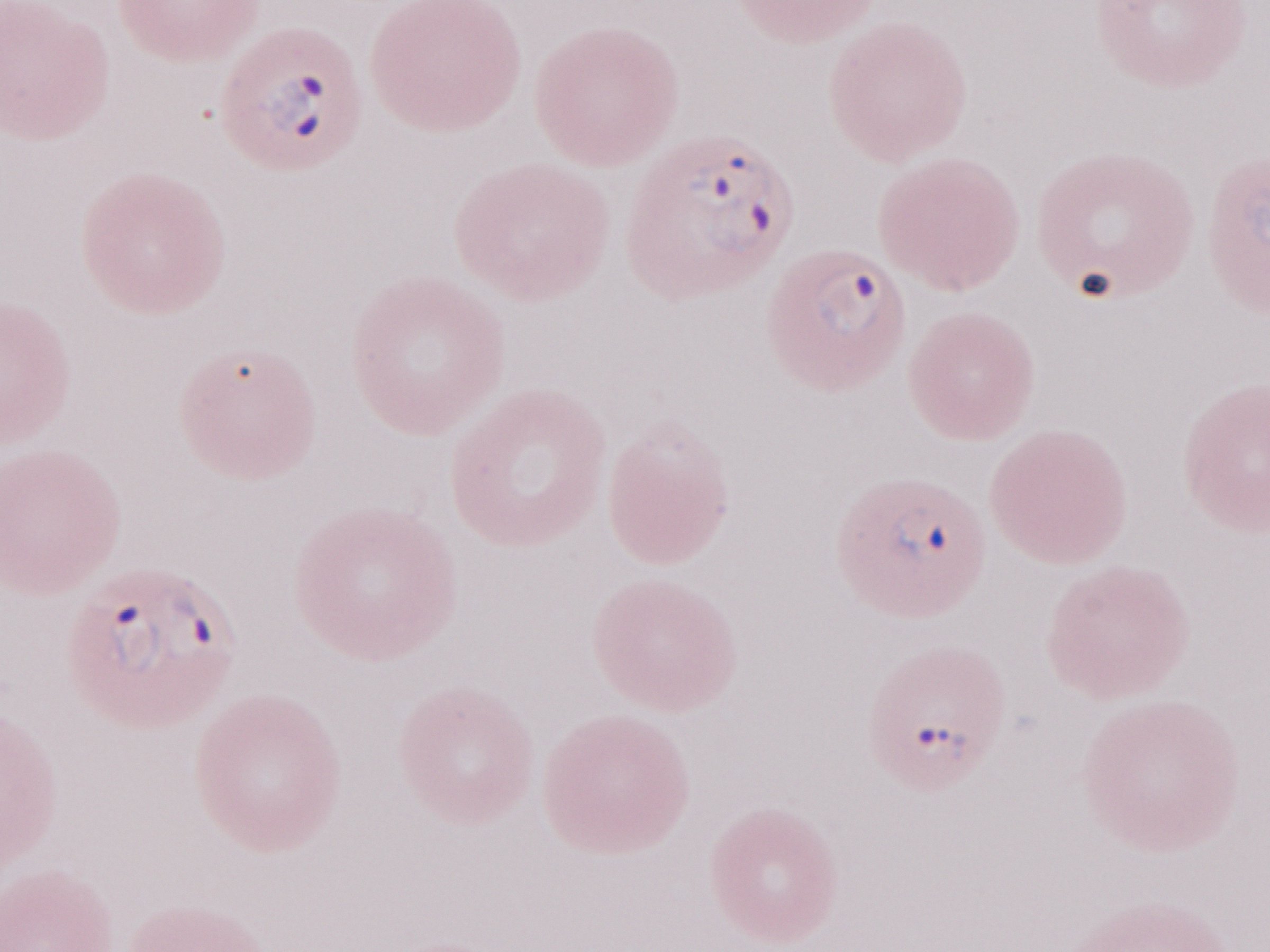 Olympus BX43 microscope, Olympus DP73 camera. May-Grünwald-Giemsa stain. Patient diagnosis: malaria infection. One field of this slide. Image is 1270×952 pixels. Thin peripheral-blood smear. 1,000x magnification.